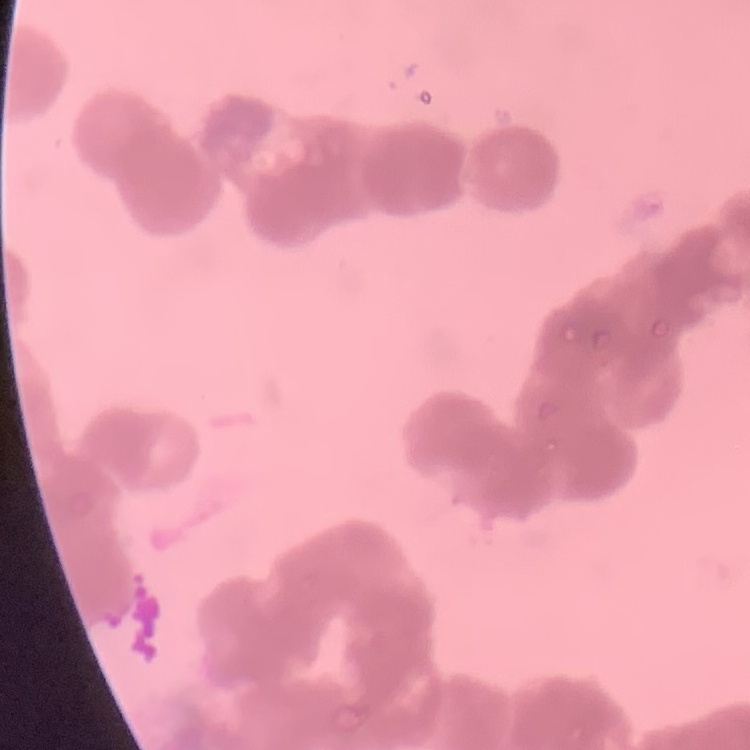 The red blood cells show rouleaux formation. Thin peripheral smear. One tile cut from a larger photomicrograph. Field's or Giemsa stain.